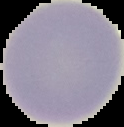
malaria status = uninfected
image type = segmented cell region with the area outside set to black
image size = 124×127 pixels
preparation = thin blood film